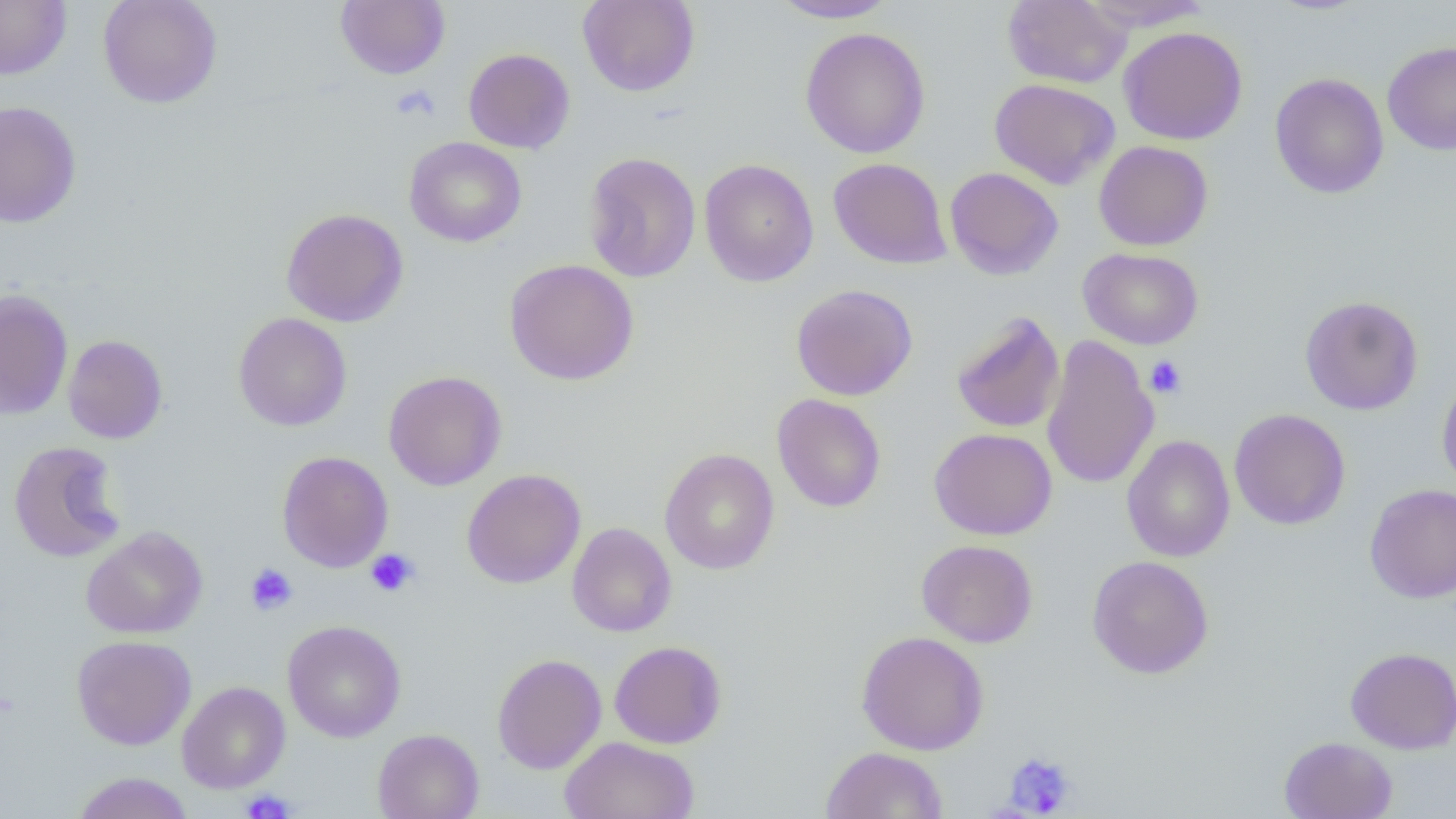 Approximate bounding boxes as (x1,y1)-(x2,y2) corner pairs in pixels. Uninfected red blood cell locations: (0,0)-(71,79), (97,0)-(223,108), (577,0)-(700,97), (770,0)-(901,23), (1002,0)-(1132,88), (1080,0)-(1214,32), (336,1)-(450,79), (1118,26)-(1247,145), (800,27)-(931,158), (1382,41)-(1456,155), (463,48)-(575,154), (1270,72)-(1389,199), (989,78)-(1120,189), (0,100)-(82,229), (404,136)-(527,247), (1094,140)-(1213,251), (583,151)-(701,283), (700,158)-(819,287), (828,158)-(952,269), (944,166)-(1063,280), (281,208)-(409,327), (1078,247)-(1204,349), (504,258)-(639,385), (791,284)-(918,401), (0,289)-(74,420), (1299,295)-(1424,415), (951,311)-(1065,434), (233,312)-(352,432), (63,334)-(168,443), (1041,334)-(1159,491), (383,370)-(507,491), (1437,371)-(1456,492), (771,393)-(886,513), (1228,408)-(1351,530), (929,427)-(1057,539), (1121,434)-(1236,562), (8,440)-(126,562), (659,449)-(779,574), (277,451)-(394,572), (461,469)-(586,589), (1364,483)-(1456,603), (567,522)-(677,637), (81,525)-(208,639), (916,539)-(1038,647), (1086,555)-(1214,679), (282,620)-(406,743), (856,631)-(990,755), (72,635)-(196,750), (609,640)-(727,749), (1345,646)-(1456,754), (492,653)-(606,774), (177,680)-(290,793), (372,729)-(484,819), (560,736)-(700,819), (1279,736)-(1397,818), (820,746)-(948,818), (71,771)-(193,819). Platelet locations: (391,85)-(440,122), (1145,355)-(1187,399), (365,549)-(419,597), (245,563)-(298,615), (1003,751)-(1077,816), (241,788)-(296,818). Slide-level diagnosis: negative for blood parasites. Single field of view. Image is 1456×819 pixels. 1000x magnification. Thin blood smear. Optical microscopy.